State which cell type is depicted.
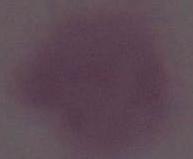

This is an erythrocyte.

{
  "modality": "micrograph",
  "magnification": "1000x"
}